Assess the morphology of the erythrocytes.
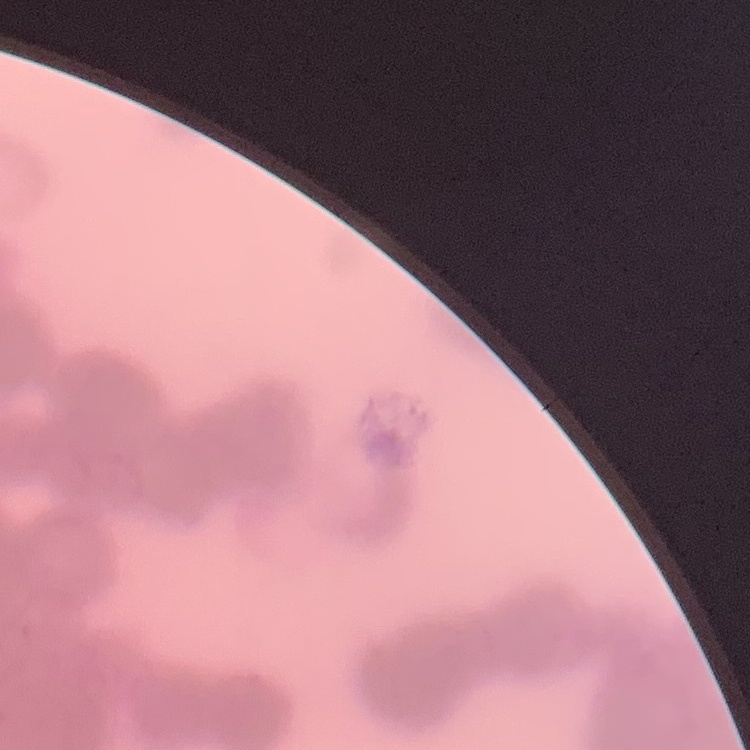

They show rouleaux formation.

Square crop of a larger photomicrograph. Stained with either Field's or Giemsa. Thin peripheral smear.